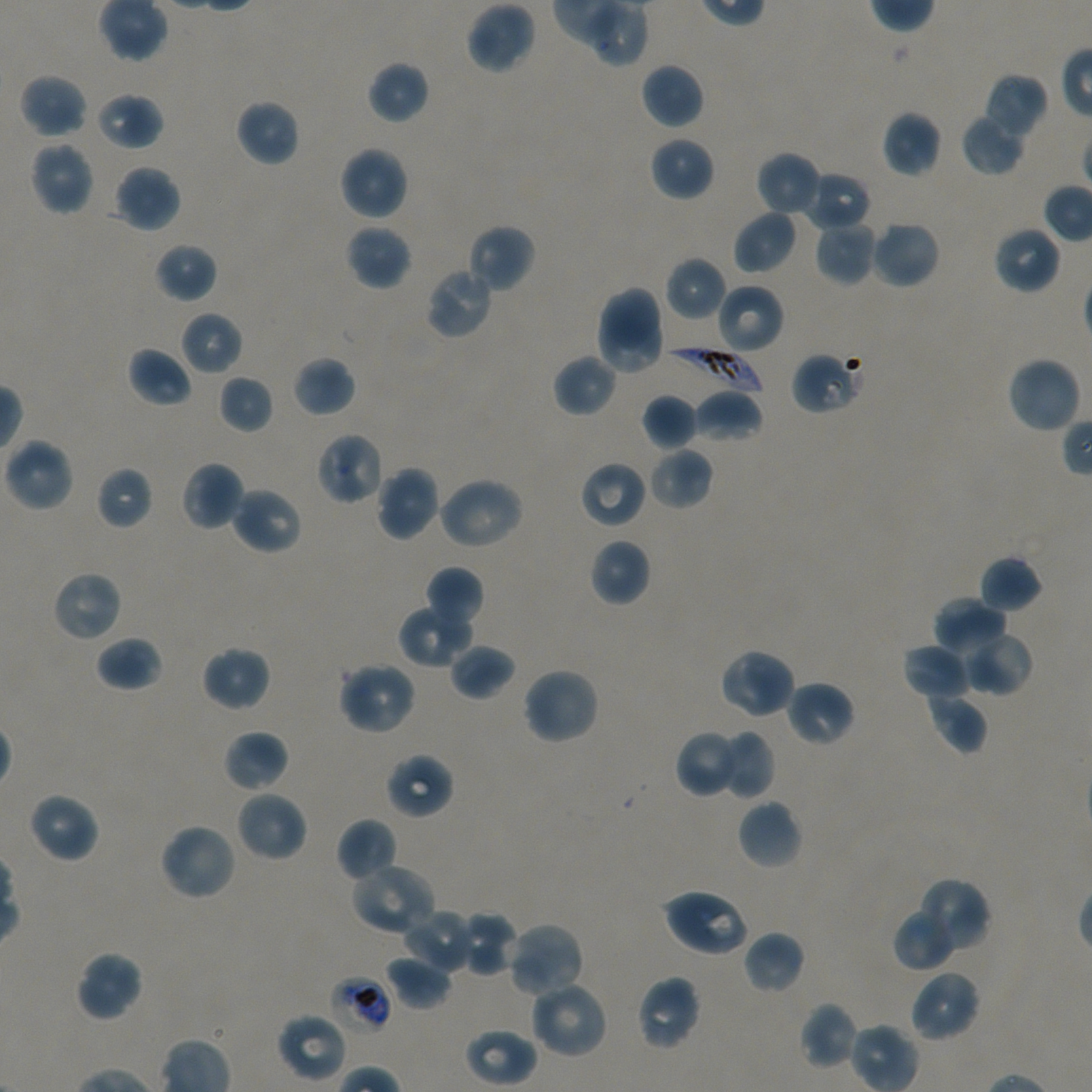

Not every red blood cell is marked.
stain = Giemsa
objective = 100x, oil immersion, numerical aperture 1.45
locations of red blood cells of indeterminate infection status = approximate bounding boxes as (x1, y1, x2, y2) in pixels: (331, 976, 393, 1034)
culture = static in-vitro Plasmodium falciparum strain NF54
locations of uninfected red blood cells = approximate bounding boxes as (x1, y1, x2, y2) in pixels: (466, 1, 536, 75), (367, 61, 430, 124), (640, 62, 704, 129), (19, 73, 89, 138), (983, 73, 1049, 138), (94, 92, 164, 151), (234, 99, 300, 166), (882, 111, 943, 178), (962, 113, 1026, 176), (649, 136, 714, 202), (29, 141, 94, 216), (338, 146, 409, 221), (756, 151, 822, 217), (113, 164, 181, 233), (803, 170, 872, 232), (732, 209, 797, 274), (814, 219, 879, 287), (870, 220, 940, 289), (345, 223, 413, 291), (466, 223, 536, 294), (993, 225, 1061, 294), (154, 242, 218, 303), (665, 256, 727, 321), (424, 266, 494, 339), (715, 283, 785, 354), (596, 285, 661, 352), (598, 308, 664, 374), (179, 311, 244, 376), (127, 346, 193, 407), (791, 351, 860, 415), (552, 354, 617, 417), (292, 356, 356, 418), (1006, 356, 1082, 435), (218, 374, 274, 434), (692, 389, 763, 443), (641, 393, 699, 451), (315, 431, 386, 505), (3, 438, 73, 512), (647, 446, 714, 510), (181, 460, 244, 532), (579, 460, 647, 529), (96, 466, 153, 530), (376, 466, 441, 541), (437, 476, 524, 550), (230, 486, 302, 555), (589, 538, 651, 606), (977, 555, 1043, 614), (424, 566, 485, 630), (52, 570, 123, 642), (933, 596, 1008, 657), (398, 604, 475, 668), (960, 629, 1033, 696), (95, 636, 164, 692), (901, 642, 970, 699), (448, 643, 515, 702), (201, 645, 270, 711), (720, 647, 797, 720), (338, 661, 418, 735), (522, 666, 600, 745), (786, 679, 856, 747), (925, 691, 988, 754), (223, 729, 290, 792), (715, 729, 776, 800), (675, 730, 745, 799), (384, 752, 454, 820), (236, 790, 308, 862), (27, 792, 100, 863), (737, 799, 803, 870), (336, 818, 399, 883), (158, 822, 237, 901), (350, 862, 437, 935), (915, 877, 991, 955), (662, 886, 751, 958), (893, 907, 958, 972), (402, 909, 476, 974), (456, 910, 520, 977), (506, 922, 585, 1000), (743, 930, 805, 994), (75, 950, 144, 1022), (384, 956, 454, 1011), (908, 969, 981, 1042), (635, 974, 703, 1051), (528, 980, 608, 1059), (798, 1002, 860, 1070), (276, 1012, 347, 1082), (463, 1028, 538, 1086)
donor blood group = A+/O+
field of view = one from this slide
locations of infected red blood cells = approximate bounding boxes as (x1, y1, x2, y2) in pixels: (662, 345, 763, 397)
image size = 1092×1092 pixels
preparation = thin blood smear